Assess for Plasmodium parasites.
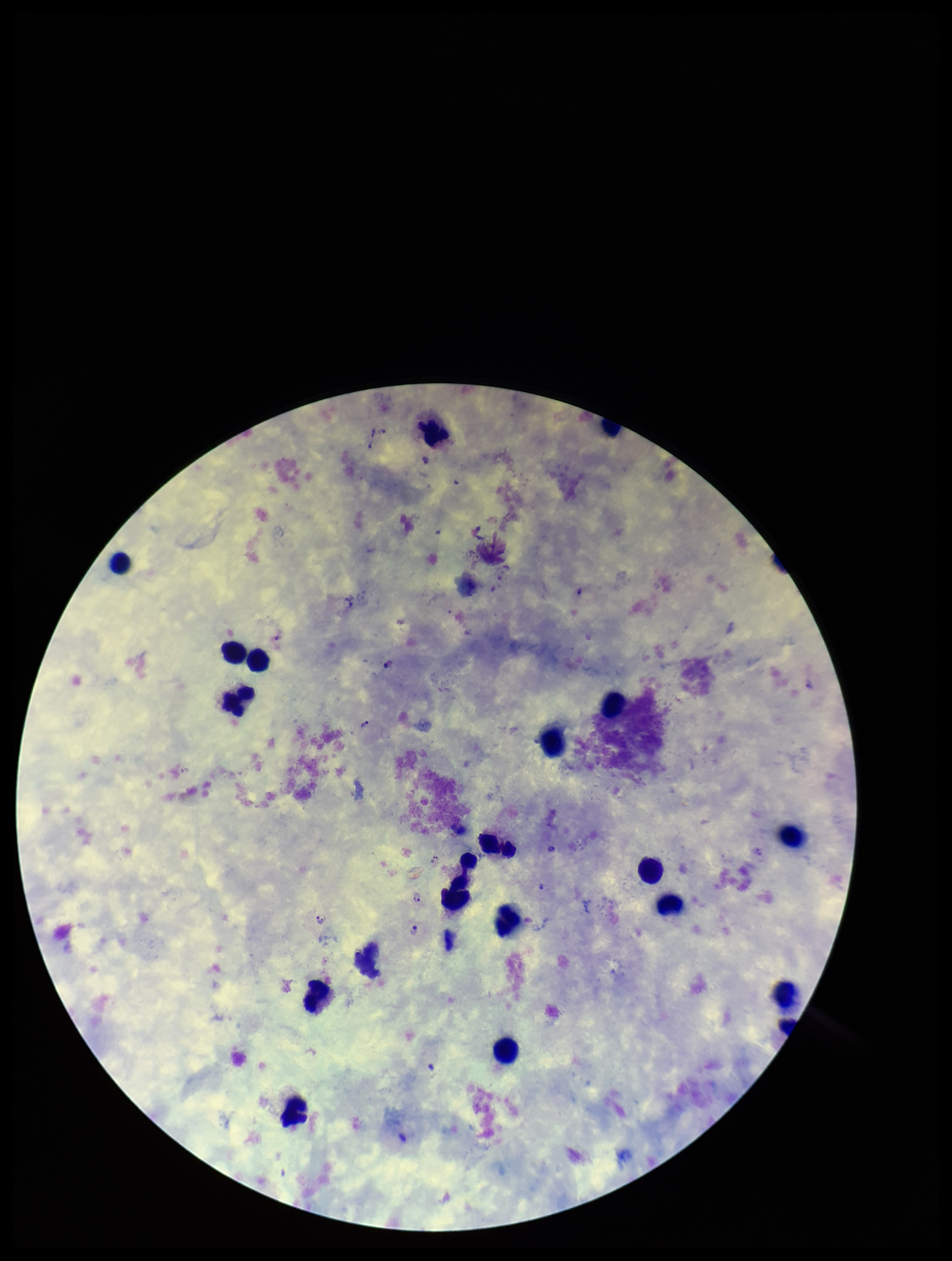

Detected.

Summary:
  - Leukocyte count: 18
  - Patient malaria status: positive
  - Image size: 952×1261 pixels
  - Preparation: thick smear
  - Species reported for this patient: Plasmodium vivax
  - Parasite count: 9
  - Capture: smartphone photograph through the microscope eyepiece
  - Field of view: one from this slide
  - Stain: Giemsa